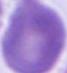
Summary:
  - Modality: micrograph
  - Magnification: 1000x
  - Identification: red blood cell